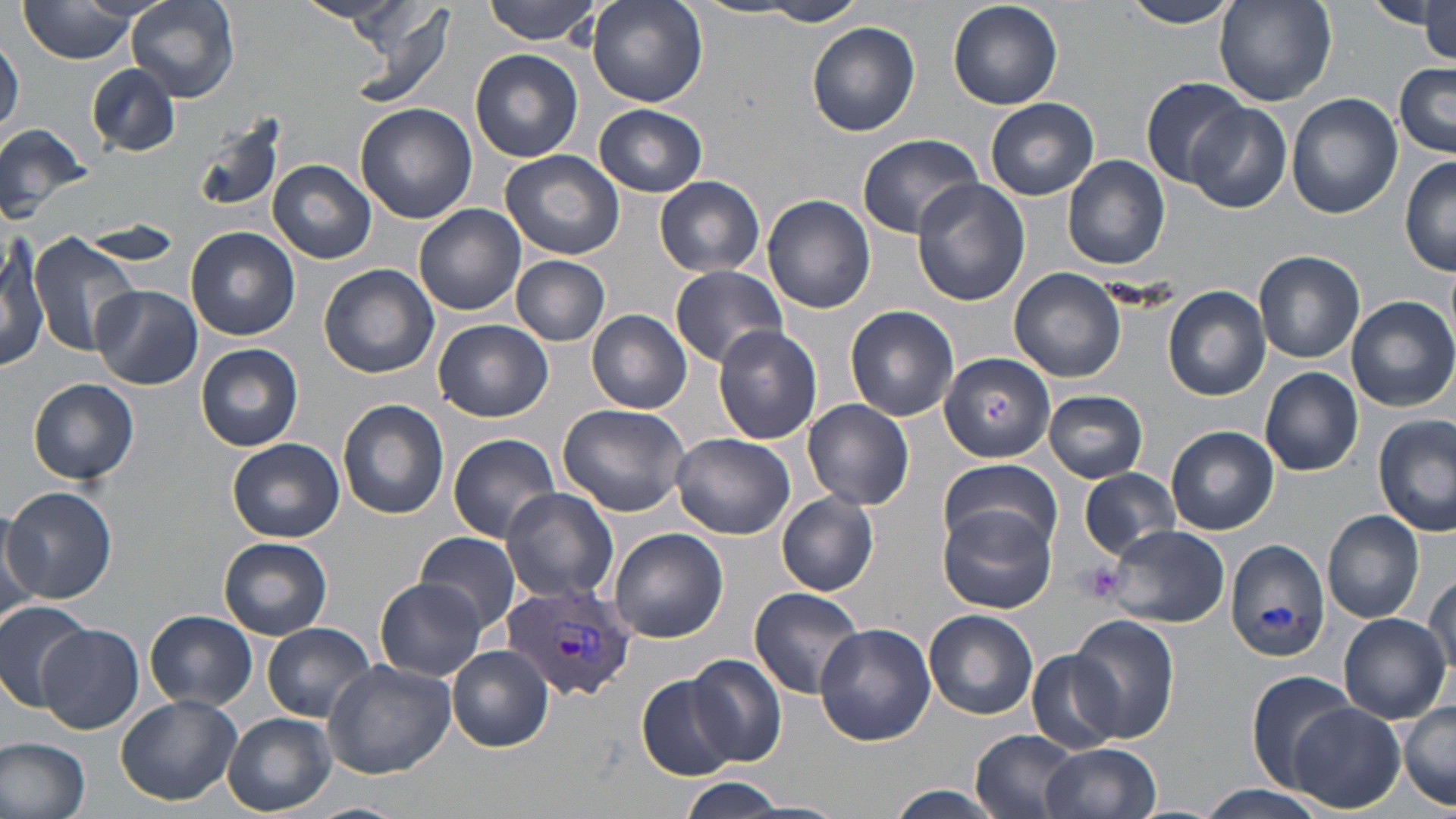
Summary:
  - Coordinate format: approximate bounding boxes as [x1, y1, x2, y2] in pixels
  - Uninfected red blood cell locations: [16, 0, 144, 63], [125, 0, 240, 107], [293, 0, 420, 29], [484, 0, 600, 44], [1121, 0, 1236, 28], [1214, 0, 1335, 107], [1366, 0, 1451, 30], [1420, 0, 1456, 60], [588, 1, 709, 107], [755, 1, 868, 25], [342, 2, 460, 110], [690, 2, 812, 20], [949, 2, 1063, 110], [91, 9, 218, 152], [807, 23, 920, 136], [2, 35, 24, 136], [471, 49, 584, 164], [1395, 61, 1455, 157], [86, 64, 179, 157], [1140, 75, 1251, 188], [1286, 93, 1402, 219], [986, 98, 1099, 201], [355, 102, 475, 224], [594, 103, 708, 197], [1186, 103, 1291, 214], [191, 112, 292, 220], [0, 121, 95, 229], [857, 132, 982, 239], [501, 149, 623, 259], [1061, 155, 1169, 271], [1400, 157, 1456, 276], [268, 161, 375, 263], [655, 177, 766, 277], [912, 177, 1030, 306], [763, 194, 877, 314], [414, 203, 526, 316], [70, 223, 184, 265], [185, 227, 299, 341], [0, 231, 47, 372], [29, 232, 139, 355], [1254, 250, 1365, 362], [511, 255, 611, 345], [319, 263, 439, 378], [669, 264, 788, 367], [1010, 266, 1126, 381], [91, 285, 203, 390], [1162, 285, 1271, 401], [1348, 295, 1456, 411], [846, 306, 958, 421], [587, 310, 692, 414], [433, 319, 553, 422], [711, 325, 825, 445], [196, 344, 302, 452], [940, 352, 1054, 462], [1260, 367, 1363, 476], [29, 379, 139, 485], [1044, 389, 1148, 483], [337, 399, 450, 519], [804, 399, 914, 510], [558, 401, 693, 516], [1374, 417, 1454, 537], [1166, 427, 1278, 535], [448, 432, 560, 542], [670, 432, 796, 540], [228, 438, 344, 542], [941, 457, 1060, 555], [1079, 467, 1180, 559], [3, 485, 117, 604], [501, 487, 621, 605], [776, 493, 878, 595], [938, 504, 1056, 614], [1322, 510, 1426, 623], [0, 516, 39, 629], [1105, 524, 1230, 628], [608, 528, 728, 644], [416, 531, 520, 635], [219, 537, 333, 639], [1226, 539, 1331, 661], [1425, 572, 1456, 687], [374, 579, 485, 680], [748, 586, 867, 699], [0, 602, 93, 708], [925, 610, 1039, 719], [145, 611, 257, 709], [1338, 614, 1450, 722], [1067, 615, 1180, 741], [262, 622, 377, 722], [814, 623, 936, 747], [36, 624, 144, 735], [446, 647, 553, 752], [1027, 649, 1125, 754], [686, 653, 788, 767], [323, 661, 459, 780], [1246, 670, 1358, 788], [637, 675, 738, 778], [116, 694, 243, 805], [1397, 702, 1456, 810], [1288, 704, 1405, 814], [223, 713, 336, 814], [971, 730, 1085, 819], [0, 736, 91, 818], [1041, 743, 1160, 819], [678, 778, 791, 817], [880, 786, 1012, 819], [1191, 786, 1332, 819], [303, 800, 411, 818]
  - Plasmodium vivax-infected red blood cell locations: [503, 581, 637, 697]
  - Platelet locations: [1078, 561, 1125, 604]
  - Slide-level diagnosis: Plasmodium vivax
  - Image size: 1456×819 pixels
  - Preparation: thin blood smear
  - Stain: May-Grünwald-Giemsa
  - Field of view: single
  - Magnification: 1000x
  - Modality: optical microscopy